Assess this cell for malaria.
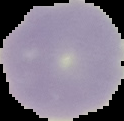

Uninfected.

image size = 124×121 pixels
image type = segmented cell region on a black background
preparation = thin blood film